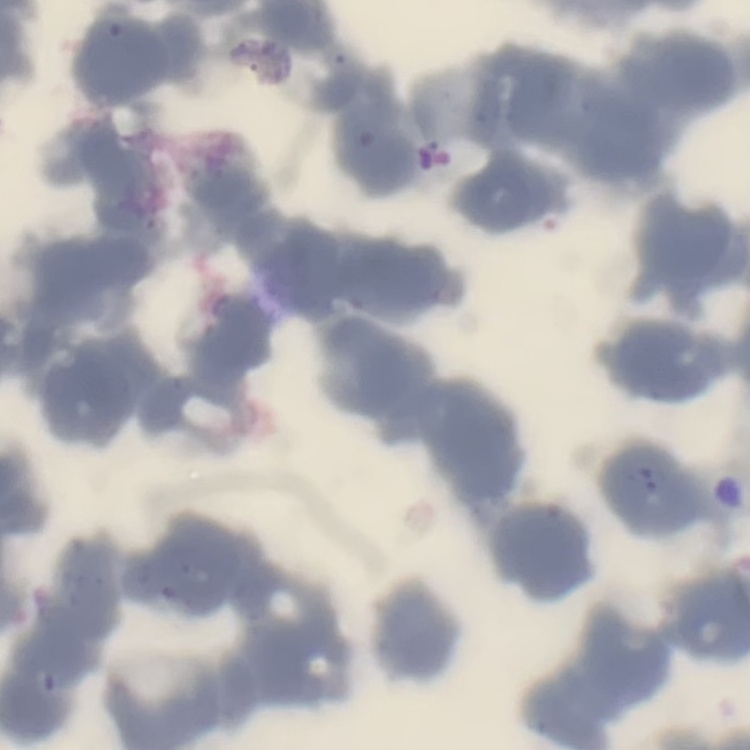

red blood cell morphology = rouleaux formation
stain = Field's or Giemsa
preparation = thin blood smear
image type = square crop of a larger photomicrograph